Assess this cell for malaria.
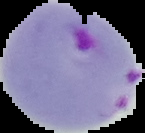
Parasitized.

Summary:
  - Image size: 145×133 pixels
  - Image type: segmented cell region on a black background
  - Preparation: thin blood smear